Outline each Plasmodium falciparum-infected red blood cell.
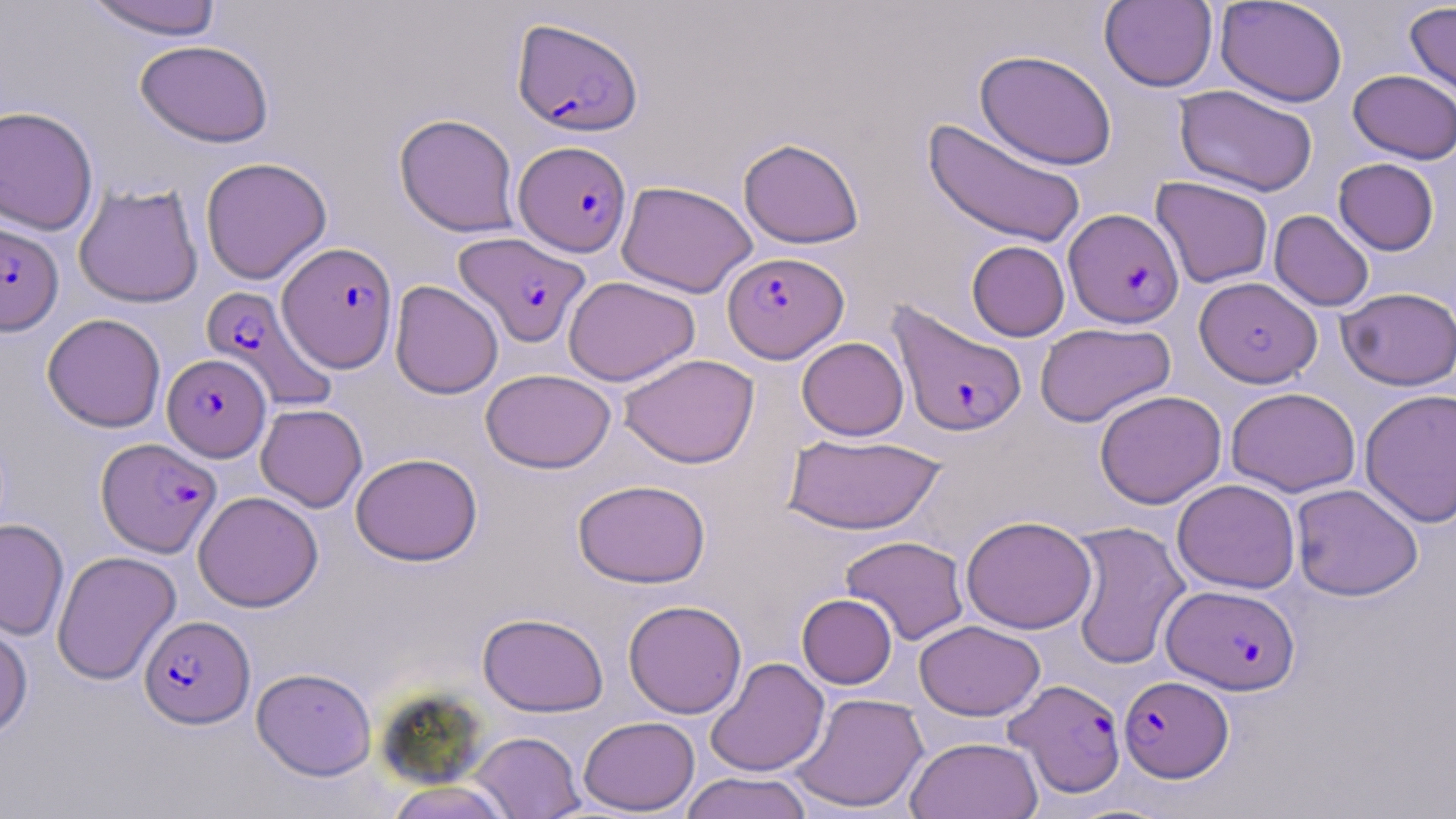
Approximate bounding boxes as named x1/y1/x2/y2 corners in pixels.
Plasmodium falciparum-infected red blood cells: (x1=512, y1=17, x2=642, y2=136), (x1=514, y1=140, x2=632, y2=256), (x1=1064, y1=208, x2=1183, y2=328), (x1=0, y1=222, x2=64, y2=336), (x1=453, y1=231, x2=590, y2=348), (x1=278, y1=242, x2=398, y2=372), (x1=723, y1=251, x2=848, y2=363), (x1=1195, y1=276, x2=1321, y2=388), (x1=201, y1=285, x2=337, y2=411), (x1=887, y1=301, x2=1028, y2=437), (x1=162, y1=353, x2=271, y2=461), (x1=96, y1=437, x2=221, y2=556), (x1=1162, y1=584, x2=1300, y2=695), (x1=140, y1=614, x2=254, y2=728), (x1=1119, y1=675, x2=1233, y2=781), (x1=1005, y1=678, x2=1126, y2=798).

Summary:
  - Uninfected red blood cell locations: (x1=83, y1=0, x2=223, y2=40), (x1=1214, y1=0, x2=1348, y2=107), (x1=1099, y1=1, x2=1218, y2=92), (x1=1404, y1=1, x2=1456, y2=105), (x1=135, y1=39, x2=273, y2=148), (x1=975, y1=49, x2=1118, y2=170), (x1=1348, y1=69, x2=1456, y2=164), (x1=1174, y1=84, x2=1318, y2=196), (x1=0, y1=105, x2=99, y2=235), (x1=394, y1=113, x2=521, y2=238), (x1=923, y1=117, x2=1086, y2=248), (x1=738, y1=137, x2=865, y2=249), (x1=200, y1=156, x2=332, y2=284), (x1=1333, y1=158, x2=1439, y2=255), (x1=1151, y1=176, x2=1273, y2=288), (x1=616, y1=180, x2=758, y2=298), (x1=74, y1=183, x2=203, y2=308), (x1=1269, y1=210, x2=1374, y2=311), (x1=966, y1=240, x2=1070, y2=341), (x1=563, y1=276, x2=700, y2=386), (x1=390, y1=280, x2=504, y2=399), (x1=1337, y1=287, x2=1456, y2=391), (x1=42, y1=313, x2=166, y2=432), (x1=1035, y1=322, x2=1175, y2=427), (x1=796, y1=337, x2=909, y2=440), (x1=618, y1=353, x2=759, y2=468), (x1=481, y1=369, x2=616, y2=473), (x1=1226, y1=387, x2=1360, y2=497), (x1=1359, y1=388, x2=1456, y2=528), (x1=1094, y1=389, x2=1226, y2=509), (x1=256, y1=403, x2=367, y2=512), (x1=782, y1=433, x2=945, y2=535), (x1=350, y1=452, x2=482, y2=566), (x1=573, y1=479, x2=711, y2=588), (x1=1172, y1=479, x2=1300, y2=593), (x1=1290, y1=483, x2=1423, y2=601), (x1=193, y1=491, x2=323, y2=612), (x1=961, y1=516, x2=1097, y2=634), (x1=0, y1=518, x2=69, y2=641), (x1=1067, y1=520, x2=1190, y2=670), (x1=840, y1=535, x2=969, y2=646), (x1=52, y1=550, x2=181, y2=685), (x1=797, y1=593, x2=897, y2=689), (x1=623, y1=599, x2=747, y2=719), (x1=478, y1=612, x2=608, y2=717), (x1=0, y1=613, x2=33, y2=741), (x1=914, y1=620, x2=1045, y2=721), (x1=705, y1=657, x2=829, y2=777), (x1=252, y1=667, x2=377, y2=780), (x1=789, y1=692, x2=928, y2=813), (x1=578, y1=716, x2=700, y2=815), (x1=469, y1=731, x2=585, y2=818), (x1=906, y1=736, x2=1043, y2=819), (x1=679, y1=771, x2=813, y2=819), (x1=384, y1=779, x2=514, y2=819)
  - Slide-level diagnosis: Plasmodium falciparum
  - Preparation: thin blood film
  - Modality: light microscopy
  - Magnification: 1000x
  - Field of view: one of a larger specimen
  - Stain: May-Grünwald-Giemsa
  - Image size: 1456×819 pixels